Assess the morphology of the erythrocytes.
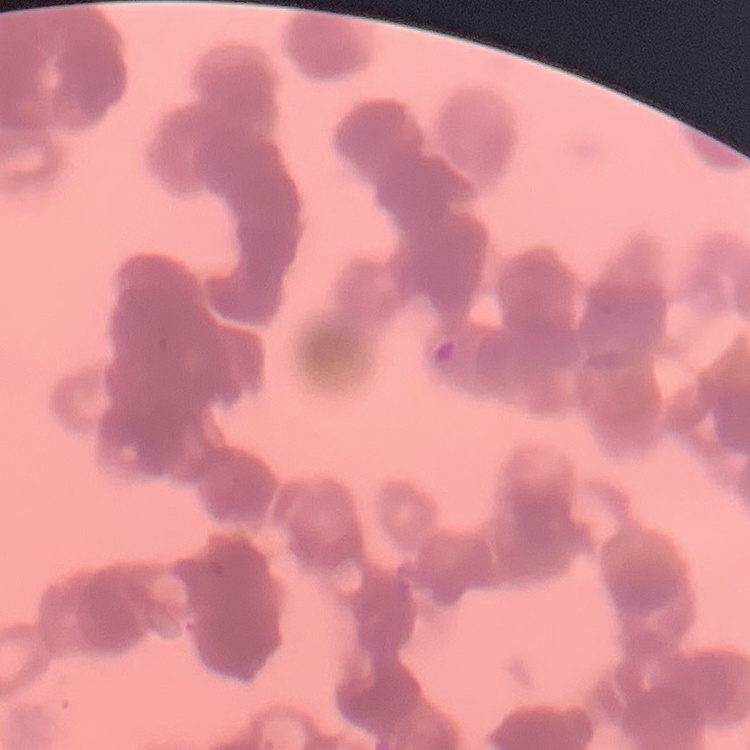

Rouleaux formation.

Summary:
  - Image type: square crop of a larger photomicrograph
  - Preparation: thin peripheral smear
  - Stain: Field's or Giemsa